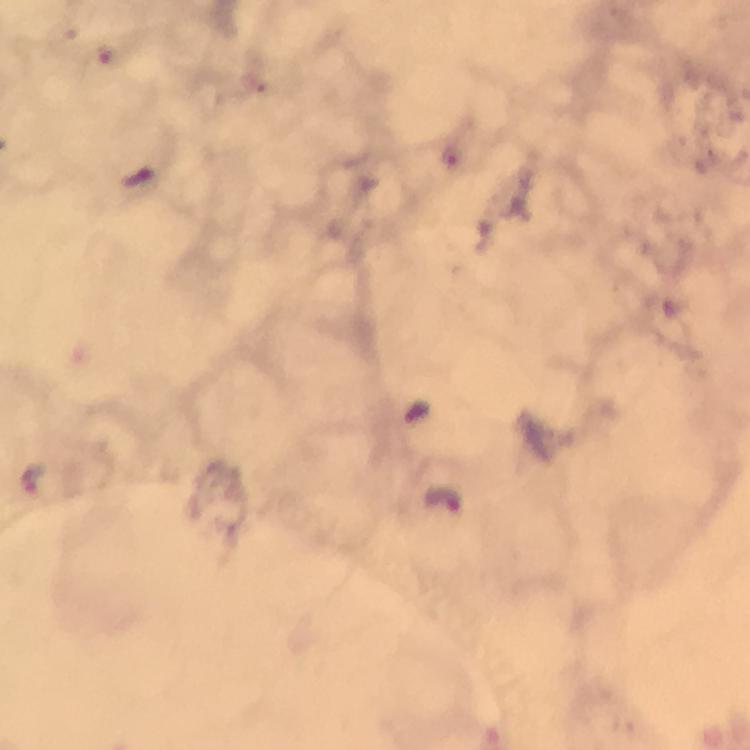
image size = 750×750 pixels
cropped from = a single field of view
stain = Giemsa
capture = smartphone photograph through a microscope
immersion oil = used
malaria parasite locations = approximate centers as (x, y) in pixels: (451, 158), (417, 412), (32, 478), (449, 499)
preparation = thick blood smear
magnification = 100x
context = from a diagnostic examination for malaria